Report the malaria status of this cell.
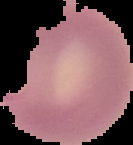

Parasitized.

Summary:
  - Image size: 133×145 pixels
  - Image type: cell region segmented out of the field of view; surrounding area masked to black
  - Preparation: thin blood film